Locate every Plasmodium parasite.
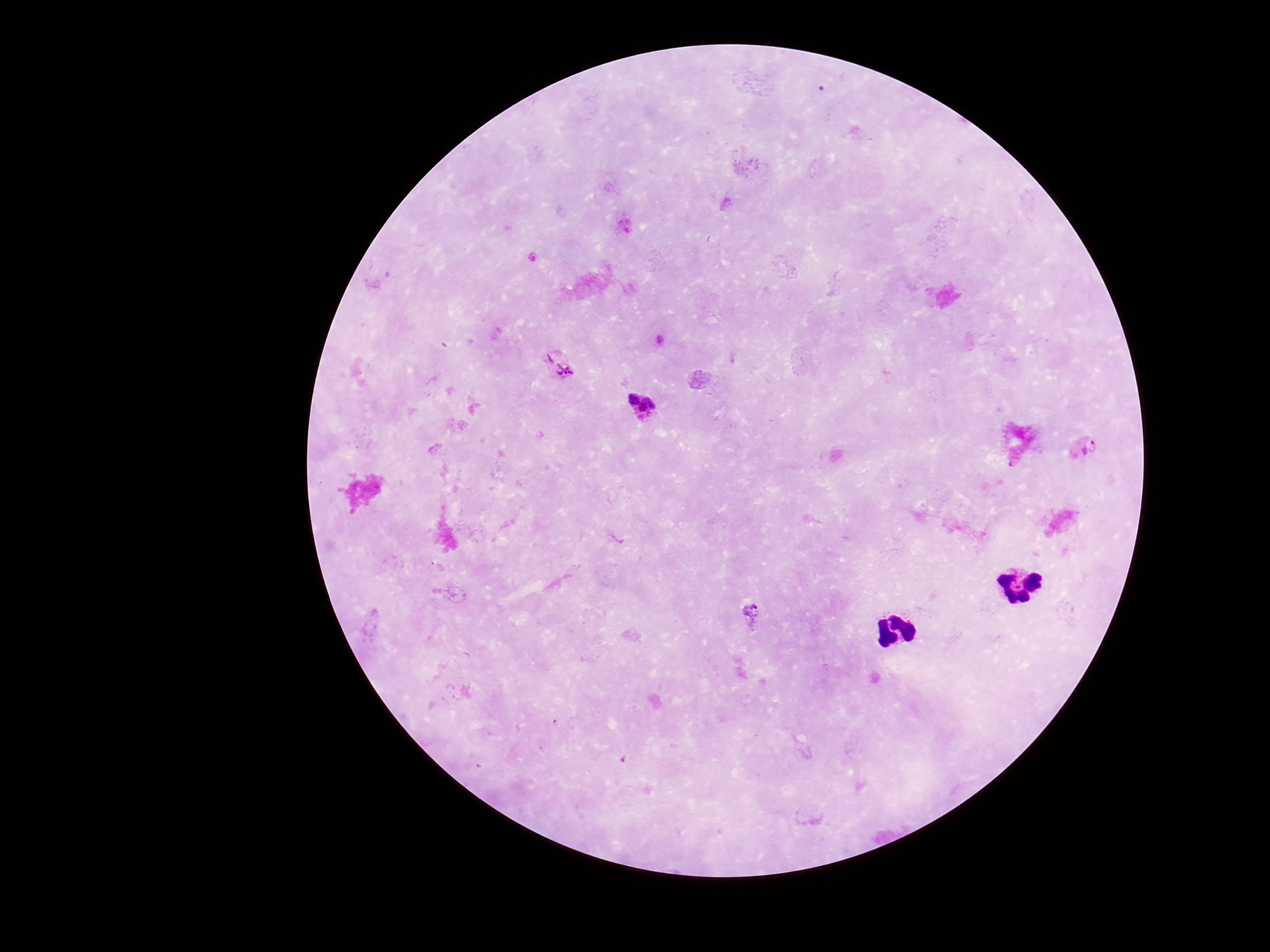
Approximate object centers, in pixels from the top-left corner.
Plasmodium parasites: (x=558, y=363), (x=641, y=405), (x=1084, y=446), (x=751, y=615).

field of view = single
capture = smartphone camera through the microscope eyepiece
patient malaria status = positive
stain = Giemsa
preparation = thick peripheral-blood smear
image size = 1270×952 pixels
magnification = 100x